Name the parasite shown.
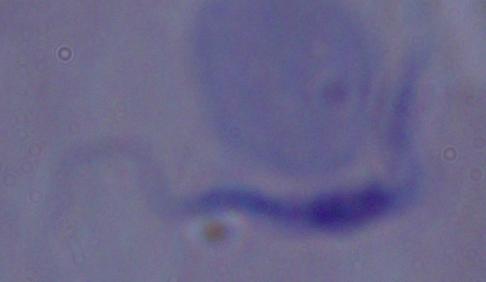
A trypanosome.

magnification = 1000x
modality = micrograph